Assess this cell for malaria.
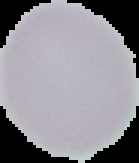
It is uninfected.

From a thin blood smear. Cell region segmented out of the field of view; the surrounding area is masked to black. Image is 139×163 pixels.